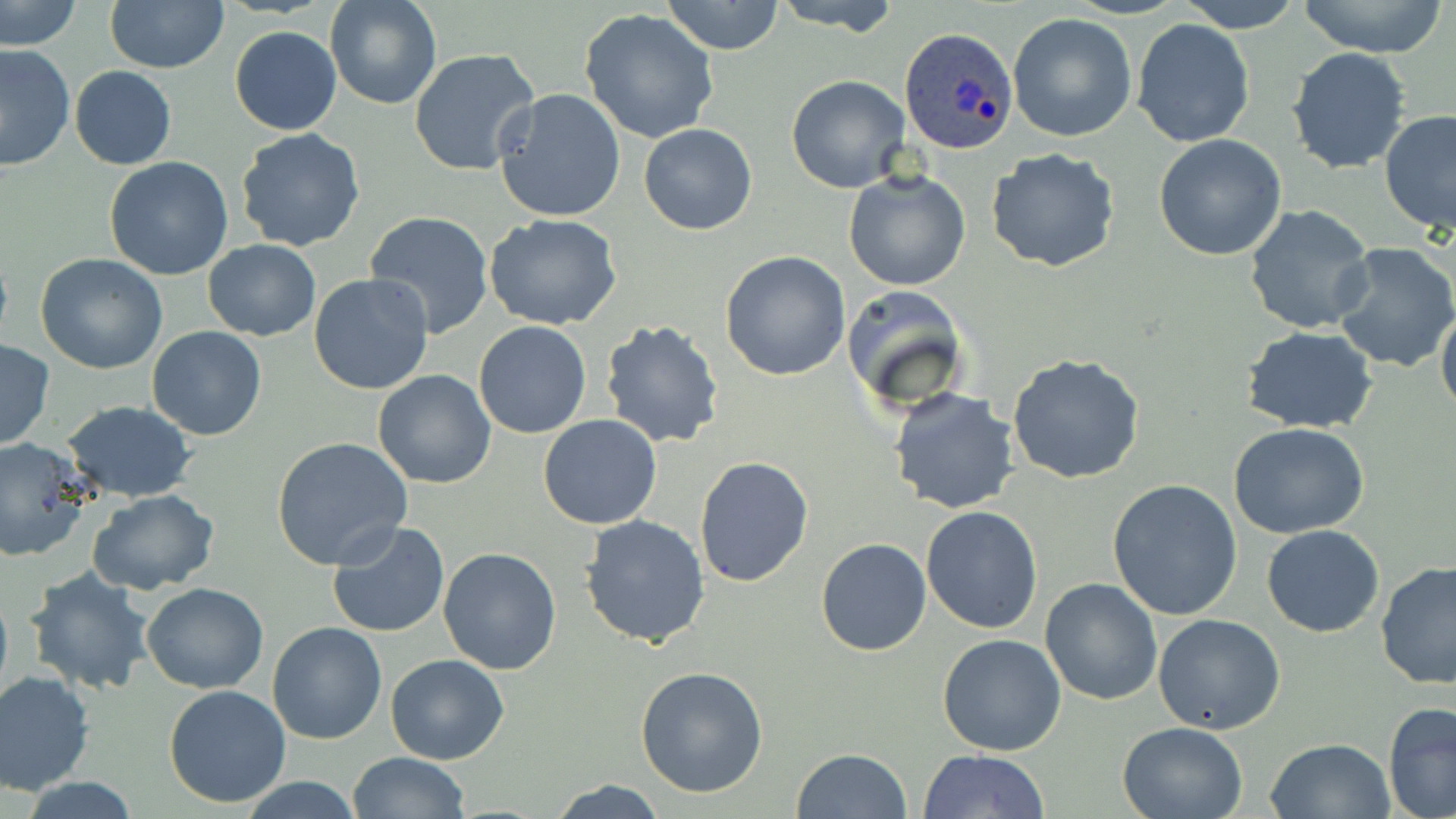
Summary:
  - Coordinate format: approximate bounding boxes as (x1,y1)-(x2,y2) corner pairs in pixels
  - Plasmodium ovale-infected red blood cell locations: (900,30)-(1019,153)
  - Uninfected red blood cell locations: (0,0)-(80,52), (105,0)-(229,72), (324,0)-(444,109), (663,0)-(784,55), (767,0)-(903,33), (1175,0)-(1305,32), (1294,0)-(1452,59), (579,8)-(720,145), (1007,12)-(1137,142), (1132,18)-(1255,148), (229,26)-(342,135), (0,43)-(77,172), (1286,46)-(1413,175), (409,48)-(541,178), (70,67)-(176,169), (786,75)-(910,192), (493,88)-(627,225), (1379,109)-(1456,236), (639,124)-(757,234), (235,127)-(366,252), (1155,132)-(1289,260), (985,148)-(1119,274), (105,156)-(234,280), (843,169)-(972,291), (1244,203)-(1379,336), (364,211)-(495,338), (484,214)-(624,330), (204,239)-(320,340), (1333,241)-(1456,375), (720,250)-(852,381), (35,254)-(168,374), (309,272)-(435,394), (1436,299)-(1456,423), (600,318)-(728,449), (473,321)-(593,438), (148,326)-(266,440), (1242,327)-(1381,434), (0,340)-(54,452), (1008,352)-(1148,485), (372,369)-(496,489), (888,388)-(1022,515), (901,391)-(1029,637), (60,401)-(197,502), (538,414)-(663,530), (1228,421)-(1371,537), (270,435)-(413,569), (0,438)-(89,561), (694,455)-(814,589), (1107,478)-(1243,621), (88,490)-(221,594), (919,504)-(1043,635), (579,514)-(713,648), (327,520)-(450,639), (1263,524)-(1384,638), (815,536)-(932,656), (439,548)-(563,675), (1375,560)-(1456,690), (24,566)-(155,696), (1040,578)-(1162,704), (0,579)-(13,709), (142,582)-(269,693), (1153,613)-(1286,735), (266,621)-(387,745), (937,633)-(1067,755), (384,654)-(509,765), (635,665)-(769,797), (0,671)-(94,795), (163,685)-(293,808), (1383,702)-(1456,819), (1118,721)-(1248,818), (1267,738)-(1395,819), (791,747)-(911,819), (347,750)-(471,819), (918,750)-(1050,818), (238,777)-(366,817), (19,778)-(143,818), (549,779)-(667,818)
  - Slide-level diagnosis: Plasmodium ovale
  - Image size: 1456×819 pixels
  - Magnification: 1000x
  - Modality: optical microscopy
  - Stain: May-Grünwald-Giemsa
  - Preparation: thin blood film
  - Field of view: one of a larger specimen